Locate every Plasmodium malariae-infected red blood cell.
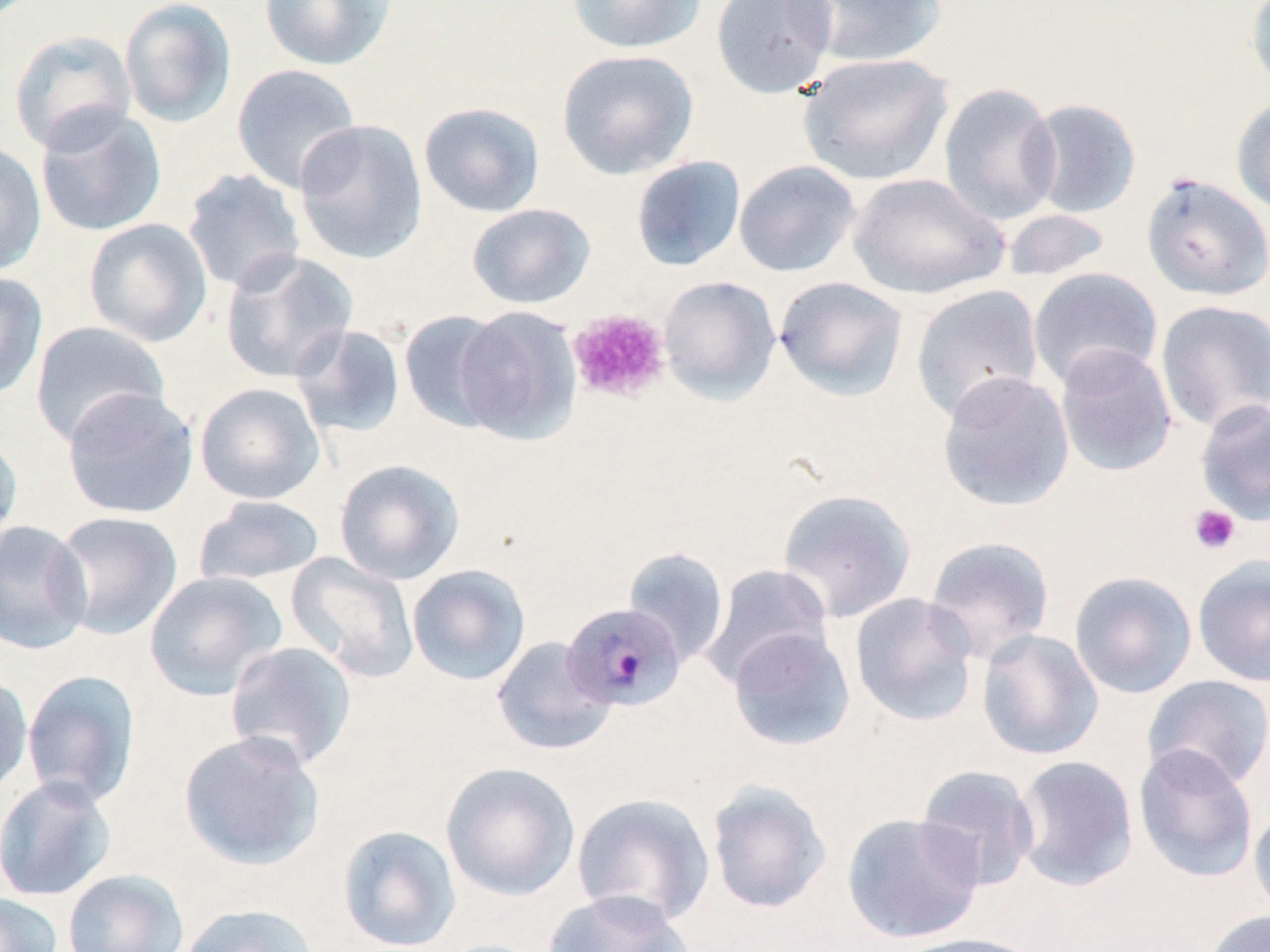
Approximate bounding boxes as named x1/y1/x2/y2 corners in pixels.
Plasmodium malariae-infected red blood cells: (x1=561, y1=601, x2=686, y2=712).

slide-level diagnosis = Plasmodium malariae
platelet locations = approximate bounding boxes as named x1/y1/x2/y2 corners in pixels: (x1=568, y1=308, x2=670, y2=403), (x1=1188, y1=504, x2=1241, y2=554)
modality = optical microscopy
field of view = one of a larger specimen
uninfected red blood cell locations = approximate bounding boxes as named x1/y1/x2/y2 corners in pixels: (x1=119, y1=0, x2=237, y2=129), (x1=258, y1=0, x2=396, y2=71), (x1=564, y1=0, x2=706, y2=55), (x1=710, y1=0, x2=838, y2=100), (x1=794, y1=0, x2=948, y2=68), (x1=1245, y1=1, x2=1270, y2=96), (x1=8, y1=29, x2=138, y2=155), (x1=557, y1=49, x2=699, y2=180), (x1=798, y1=52, x2=953, y2=186), (x1=231, y1=63, x2=363, y2=195), (x1=938, y1=82, x2=1062, y2=225), (x1=1231, y1=95, x2=1270, y2=219), (x1=1024, y1=98, x2=1143, y2=219), (x1=418, y1=102, x2=546, y2=218), (x1=35, y1=104, x2=167, y2=237), (x1=293, y1=119, x2=428, y2=265), (x1=0, y1=140, x2=47, y2=277), (x1=631, y1=155, x2=746, y2=272), (x1=734, y1=160, x2=861, y2=277), (x1=182, y1=168, x2=306, y2=294), (x1=1140, y1=171, x2=1270, y2=302), (x1=846, y1=172, x2=1009, y2=300), (x1=467, y1=203, x2=596, y2=309), (x1=1002, y1=208, x2=1113, y2=282), (x1=83, y1=217, x2=213, y2=347), (x1=219, y1=250, x2=359, y2=384), (x1=1028, y1=267, x2=1163, y2=391), (x1=0, y1=271, x2=48, y2=401), (x1=658, y1=275, x2=781, y2=404), (x1=774, y1=276, x2=909, y2=401), (x1=911, y1=284, x2=1044, y2=422), (x1=1155, y1=299, x2=1270, y2=432), (x1=453, y1=305, x2=582, y2=445), (x1=399, y1=309, x2=512, y2=431), (x1=29, y1=320, x2=170, y2=447), (x1=290, y1=324, x2=406, y2=439), (x1=1054, y1=343, x2=1177, y2=477), (x1=936, y1=370, x2=1074, y2=512), (x1=195, y1=382, x2=326, y2=505), (x1=61, y1=387, x2=199, y2=520), (x1=1195, y1=398, x2=1270, y2=526), (x1=0, y1=428, x2=23, y2=553), (x1=333, y1=458, x2=465, y2=585), (x1=777, y1=488, x2=917, y2=623), (x1=193, y1=494, x2=325, y2=587), (x1=49, y1=510, x2=183, y2=640), (x1=0, y1=519, x2=93, y2=655), (x1=923, y1=535, x2=1055, y2=662), (x1=622, y1=546, x2=730, y2=666), (x1=286, y1=552, x2=419, y2=683), (x1=1192, y1=554, x2=1270, y2=687), (x1=698, y1=563, x2=832, y2=689), (x1=406, y1=564, x2=531, y2=686), (x1=144, y1=571, x2=287, y2=700), (x1=1069, y1=571, x2=1198, y2=699), (x1=850, y1=592, x2=979, y2=727), (x1=727, y1=627, x2=856, y2=752), (x1=977, y1=628, x2=1104, y2=761), (x1=491, y1=636, x2=617, y2=756), (x1=224, y1=641, x2=357, y2=772), (x1=21, y1=670, x2=140, y2=809), (x1=0, y1=672, x2=33, y2=798), (x1=1142, y1=674, x2=1270, y2=791), (x1=178, y1=730, x2=326, y2=871), (x1=1133, y1=744, x2=1258, y2=882), (x1=1012, y1=754, x2=1139, y2=892), (x1=441, y1=762, x2=581, y2=901), (x1=915, y1=764, x2=1040, y2=891), (x1=0, y1=776, x2=117, y2=902), (x1=706, y1=780, x2=832, y2=914), (x1=571, y1=792, x2=715, y2=927), (x1=1249, y1=806, x2=1270, y2=922), (x1=842, y1=811, x2=985, y2=944), (x1=337, y1=824, x2=461, y2=951), (x1=62, y1=869, x2=189, y2=952), (x1=542, y1=889, x2=696, y2=952), (x1=0, y1=893, x2=64, y2=952), (x1=177, y1=902, x2=318, y2=952), (x1=1204, y1=909, x2=1270, y2=952), (x1=891, y1=932, x2=1042, y2=952)
stain = May-Grünwald-Giemsa
preparation = thin blood smear
image size = 1270×952 pixels
magnification = 1000x